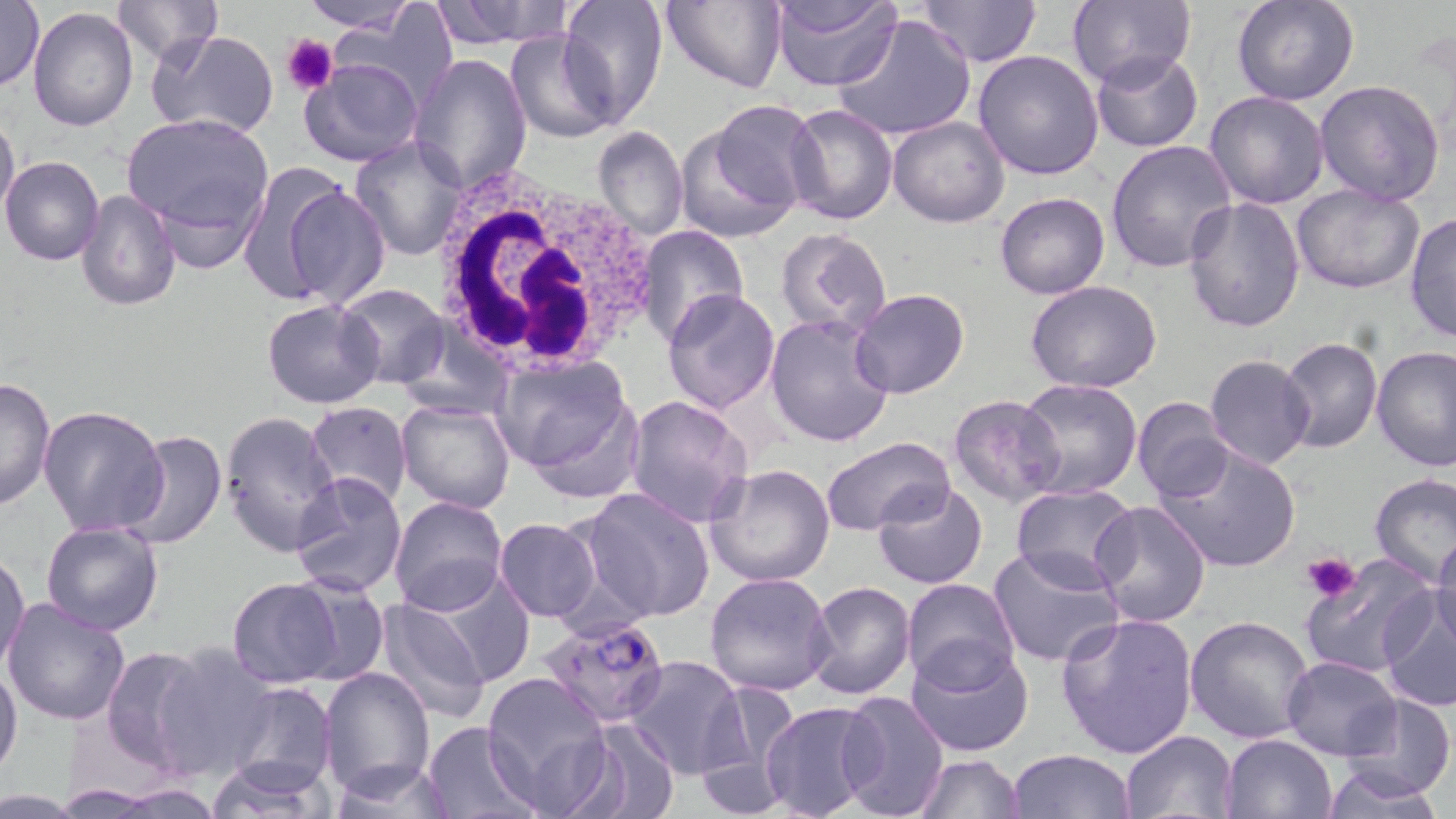

Summary:
  - Coordinate format: approximate bounding boxes as (x1, y1, x2, y2) in pixels
  - Platelet locations: (282, 32, 338, 95), (1300, 552, 1362, 604)
  - Plasmodium falciparum-infected red blood cell locations: (539, 613, 671, 727)
  - White blood cell locations: (431, 171, 664, 377)
  - Uninfected red blood cell locations: (113, 0, 222, 67), (300, 0, 420, 32), (555, 0, 668, 127), (660, 0, 787, 94), (767, 0, 903, 90), (914, 0, 1040, 67), (1067, 0, 1194, 92), (1232, 0, 1361, 106), (1, 1, 45, 92), (432, 1, 574, 49), (333, 5, 457, 109), (27, 8, 138, 131), (831, 13, 979, 141), (146, 30, 280, 139), (505, 30, 617, 143), (973, 48, 1107, 179), (1090, 51, 1204, 153), (407, 53, 532, 194), (299, 57, 425, 169), (1314, 79, 1445, 205), (1205, 90, 1330, 209), (785, 104, 898, 225), (0, 108, 20, 230), (676, 111, 814, 241), (121, 113, 274, 248), (887, 116, 1009, 227), (592, 126, 688, 242), (349, 135, 468, 261), (1107, 139, 1238, 272), (1, 155, 105, 266), (235, 162, 354, 307), (278, 183, 390, 308), (1290, 183, 1424, 294), (78, 188, 182, 311), (994, 192, 1109, 298), (1182, 197, 1306, 334), (1406, 211, 1455, 345), (638, 226, 749, 346), (774, 227, 893, 339), (1025, 279, 1162, 394), (336, 284, 451, 388), (662, 288, 781, 412), (849, 288, 970, 399), (261, 299, 385, 409), (765, 314, 897, 448), (395, 323, 513, 421), (1277, 337, 1382, 453), (1371, 344, 1454, 471), (1205, 355, 1314, 469), (496, 358, 642, 493), (0, 375, 56, 510), (1013, 376, 1146, 500), (625, 394, 753, 529), (948, 394, 1064, 507), (1132, 397, 1236, 504), (396, 400, 517, 513), (305, 402, 412, 513), (39, 405, 169, 537), (218, 410, 342, 556), (120, 430, 228, 551), (820, 437, 954, 536), (1157, 443, 1302, 574), (705, 463, 837, 587), (291, 472, 407, 598), (1368, 472, 1456, 585), (873, 481, 989, 591), (1011, 484, 1139, 589), (578, 487, 716, 623), (388, 495, 507, 616), (1088, 500, 1215, 628), (494, 517, 601, 622), (41, 522, 165, 635), (1429, 528, 1456, 650), (987, 546, 1125, 668), (1, 550, 30, 676), (1301, 555, 1437, 678), (420, 569, 535, 687), (704, 570, 836, 697), (284, 575, 389, 685), (227, 577, 345, 688), (900, 579, 1020, 691), (802, 581, 917, 699), (1377, 588, 1456, 711), (371, 597, 490, 723), (3, 598, 131, 724), (1055, 612, 1199, 760), (1186, 614, 1315, 743), (906, 643, 1034, 757), (152, 644, 278, 778), (100, 645, 208, 768), (623, 654, 749, 780), (1280, 655, 1401, 759), (0, 662, 23, 777), (318, 666, 434, 796), (481, 672, 613, 813), (698, 678, 803, 803), (228, 682, 336, 794), (835, 689, 950, 819), (1342, 693, 1454, 801), (758, 700, 885, 819), (420, 719, 545, 818), (559, 719, 682, 819), (1118, 730, 1239, 819), (1222, 734, 1338, 819), (1009, 749, 1133, 818), (913, 753, 1025, 818), (323, 757, 456, 817), (205, 758, 330, 818), (1315, 763, 1450, 817), (91, 778, 226, 816), (0, 791, 95, 816)
  - Slide-level diagnosis: Plasmodium falciparum
  - Modality: optical microscopy
  - Preparation: thin blood smear
  - Field of view: one of a larger specimen
  - Magnification: 1000x
  - Stain: May-Grünwald-Giemsa
  - Image size: 1456×819 pixels